State which cell type is depicted.
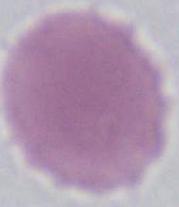
This is an erythrocyte.

Summary:
  - Magnification: 1000x
  - Modality: photomicrograph